Locate and identify every blood parasite.
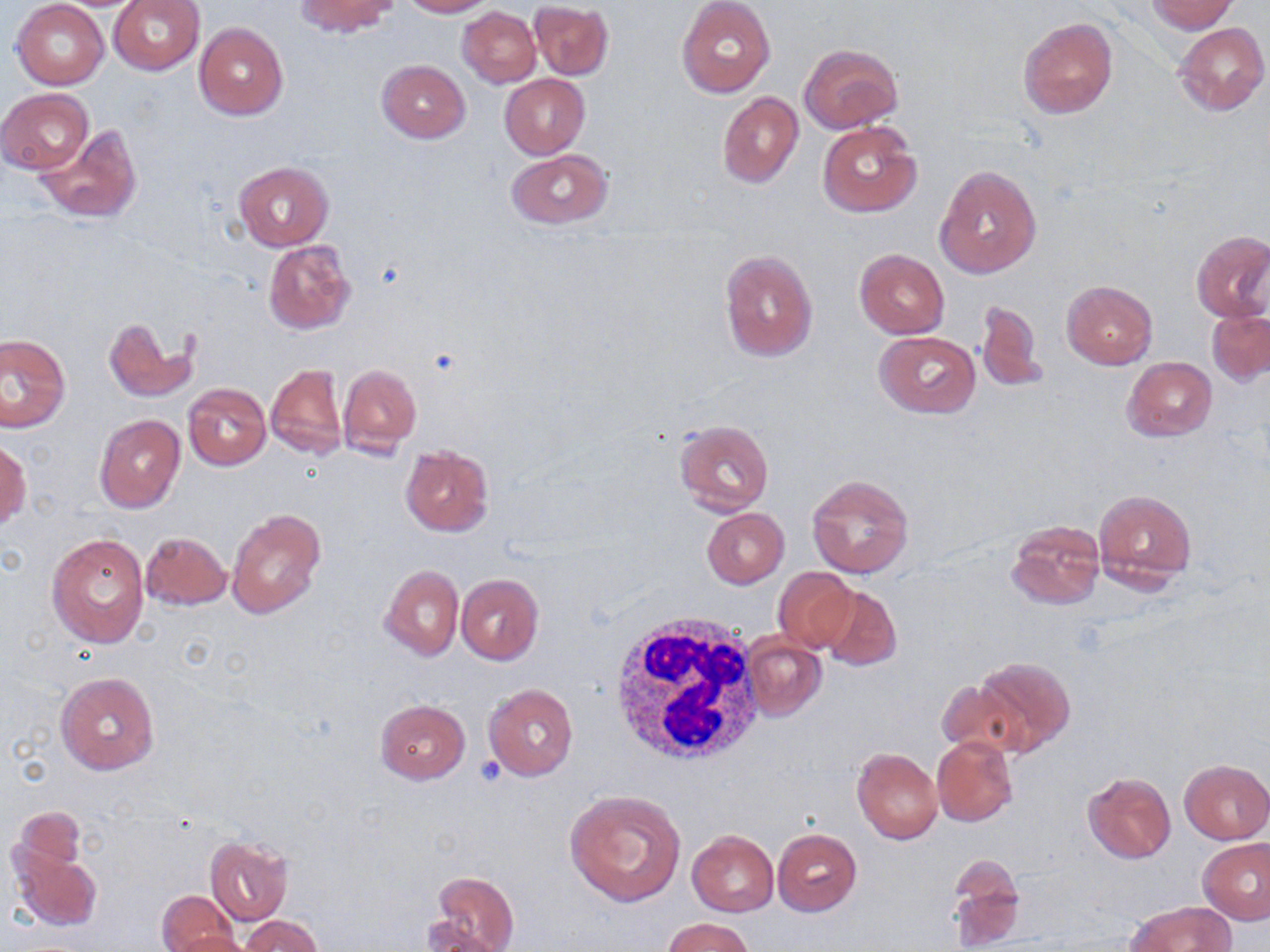
No blood parasites seen.

Summary:
  - Coordinate format: approximate bounding boxes as named x1/y1/x2/y2 corners in pixels
  - White blood cell locations: (x1=608, y1=610, x2=763, y2=769)
  - Uninfected red blood cell locations: (x1=108, y1=0, x2=204, y2=75), (x1=293, y1=0, x2=398, y2=37), (x1=400, y1=0, x2=494, y2=17), (x1=1146, y1=0, x2=1238, y2=33), (x1=12, y1=1, x2=108, y2=88), (x1=677, y1=1, x2=775, y2=98), (x1=529, y1=2, x2=613, y2=80), (x1=8, y1=3, x2=100, y2=174), (x1=457, y1=6, x2=541, y2=87), (x1=1019, y1=16, x2=1118, y2=119), (x1=194, y1=22, x2=288, y2=120), (x1=1173, y1=22, x2=1268, y2=115), (x1=799, y1=44, x2=902, y2=132), (x1=377, y1=60, x2=470, y2=142), (x1=499, y1=74, x2=589, y2=159), (x1=2, y1=88, x2=93, y2=175), (x1=717, y1=92, x2=802, y2=188), (x1=817, y1=120, x2=921, y2=218), (x1=33, y1=123, x2=143, y2=223), (x1=506, y1=149, x2=614, y2=229), (x1=234, y1=161, x2=332, y2=250), (x1=934, y1=164, x2=1042, y2=279), (x1=1192, y1=230, x2=1270, y2=323), (x1=264, y1=240, x2=357, y2=336), (x1=719, y1=249, x2=819, y2=363), (x1=855, y1=250, x2=949, y2=338), (x1=1061, y1=281, x2=1157, y2=369), (x1=975, y1=301, x2=1043, y2=393), (x1=1207, y1=309, x2=1270, y2=384), (x1=104, y1=317, x2=197, y2=404), (x1=873, y1=331, x2=981, y2=418), (x1=0, y1=334, x2=70, y2=432), (x1=1124, y1=356, x2=1215, y2=441), (x1=338, y1=363, x2=422, y2=458), (x1=266, y1=364, x2=347, y2=460), (x1=183, y1=383, x2=271, y2=470), (x1=95, y1=414, x2=185, y2=512), (x1=674, y1=419, x2=775, y2=515), (x1=1, y1=442, x2=31, y2=530), (x1=401, y1=445, x2=494, y2=535), (x1=807, y1=474, x2=914, y2=578), (x1=1094, y1=491, x2=1196, y2=587), (x1=701, y1=508, x2=790, y2=589), (x1=227, y1=509, x2=327, y2=619), (x1=1006, y1=520, x2=1106, y2=610), (x1=47, y1=532, x2=150, y2=649), (x1=140, y1=532, x2=231, y2=610), (x1=379, y1=564, x2=463, y2=661), (x1=772, y1=568, x2=857, y2=652), (x1=456, y1=573, x2=543, y2=665), (x1=818, y1=585, x2=901, y2=671), (x1=741, y1=634, x2=826, y2=721), (x1=972, y1=654, x2=1075, y2=755), (x1=55, y1=673, x2=159, y2=775), (x1=936, y1=679, x2=1027, y2=758), (x1=485, y1=684, x2=578, y2=782), (x1=376, y1=699, x2=470, y2=784), (x1=932, y1=736, x2=1019, y2=827), (x1=852, y1=748, x2=943, y2=845), (x1=1179, y1=759, x2=1270, y2=844), (x1=1082, y1=772, x2=1177, y2=864), (x1=564, y1=789, x2=687, y2=907), (x1=11, y1=806, x2=89, y2=889), (x1=773, y1=828, x2=862, y2=915), (x1=688, y1=830, x2=778, y2=916), (x1=204, y1=837, x2=292, y2=925), (x1=1198, y1=838, x2=1270, y2=925), (x1=9, y1=840, x2=102, y2=933), (x1=947, y1=858, x2=1025, y2=950), (x1=427, y1=871, x2=519, y2=952), (x1=156, y1=891, x2=240, y2=952), (x1=1127, y1=901, x2=1236, y2=952), (x1=239, y1=916, x2=324, y2=952), (x1=663, y1=917, x2=755, y2=952), (x1=419, y1=922, x2=509, y2=951), (x1=168, y1=932, x2=252, y2=952)
  - Slide-level diagnosis: no evidence of blood parasites
  - Magnification: 1000x
  - Modality: light microscopy
  - Preparation: thin blood smear
  - Image size: 1270×952 pixels
  - Stain: May-Grünwald-Giemsa
  - Field of view: one of a larger specimen